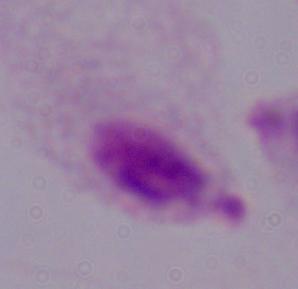

identification = trichomonad
modality = photomicrograph
magnification = 1000x